State the blood parasite species.
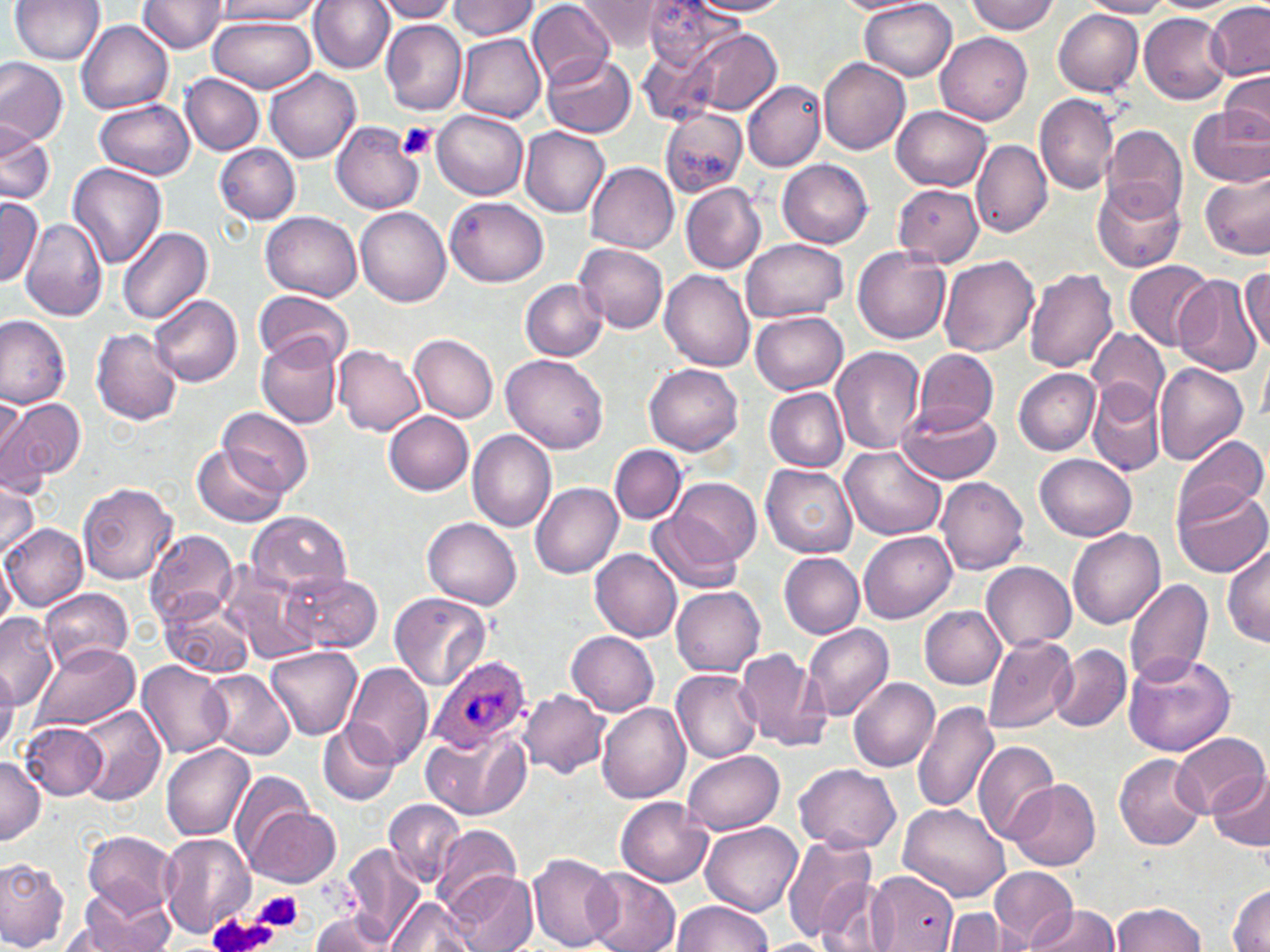
Plasmodium ovale.

Summary:
  - Coordinate format: approximate bounding boxes as (x1,y1)-(x2,y2) corner pairs in pixels
  - Platelet locations: (398,120)-(438,161), (256,889)-(303,931), (207,911)-(277,952)
  - Plasmodium ovale-infected red blood cell locations: (430,654)-(533,753)
  - Uninfected red blood cell locations: (10,0)-(105,65), (212,0)-(322,22), (310,0)-(396,73), (375,0)-(460,22), (640,0)-(735,74), (689,0)-(794,16), (859,0)-(958,80), (966,0)-(1060,36), (1082,0)-(1174,17), (137,1)-(227,54), (447,1)-(542,42), (833,1)-(932,15), (1149,1)-(1241,12), (1204,1)-(1269,81), (528,2)-(614,88), (574,2)-(684,52), (1053,9)-(1144,96), (1137,12)-(1229,103), (208,15)-(316,93), (75,19)-(173,114), (381,19)-(467,116), (669,28)-(782,119), (455,31)-(546,121), (936,33)-(1033,124), (543,53)-(636,137), (818,57)-(910,156), (0,58)-(69,148), (264,68)-(361,164), (1220,71)-(1270,144), (181,73)-(264,156), (743,78)-(826,171), (1034,94)-(1119,194), (96,98)-(196,180), (893,105)-(991,191), (1188,108)-(1270,186), (432,109)-(528,199), (661,109)-(749,197), (0,121)-(54,206), (332,121)-(423,216), (1101,123)-(1187,221), (519,125)-(610,216), (972,138)-(1052,237), (216,143)-(302,224), (777,159)-(874,247), (585,161)-(679,254), (66,162)-(168,270), (1200,165)-(1270,260), (1093,180)-(1187,273), (892,182)-(984,268), (681,183)-(767,275), (0,197)-(42,287), (446,197)-(550,288), (355,207)-(450,308), (260,212)-(362,301), (21,218)-(108,321), (118,227)-(213,326), (739,239)-(849,324), (575,244)-(670,332), (853,248)-(951,344), (939,254)-(1040,357), (1123,260)-(1211,349), (1241,267)-(1270,353), (1024,268)-(1119,374), (660,269)-(755,373), (1174,274)-(1265,375), (520,279)-(608,360), (254,291)-(352,369), (150,294)-(243,388), (751,312)-(849,395), (0,315)-(72,409), (90,327)-(183,425), (1088,327)-(1168,412), (409,332)-(498,422), (256,333)-(342,429), (334,345)-(425,437), (830,345)-(925,454), (913,348)-(1000,434), (1258,349)-(1270,429), (501,354)-(607,455), (1154,362)-(1247,466), (644,363)-(744,456), (1013,368)-(1101,454), (1088,379)-(1165,476), (763,388)-(849,472), (0,391)-(27,478), (0,396)-(85,487), (895,400)-(1002,484), (218,407)-(313,499), (384,412)-(474,495), (466,429)-(558,533), (1173,434)-(1269,528), (194,443)-(287,528), (610,445)-(686,524), (839,446)-(946,541), (1034,453)-(1136,541), (760,464)-(858,559), (663,475)-(762,574), (935,476)-(1030,575), (0,481)-(39,562), (531,482)-(623,578), (78,483)-(178,585), (1173,484)-(1268,579), (246,511)-(353,599), (650,512)-(743,594), (423,517)-(522,610), (1,523)-(87,612), (144,528)-(241,629), (860,529)-(958,624), (1067,529)-(1165,629), (1222,544)-(1269,648), (590,549)-(683,643), (779,552)-(864,638), (0,554)-(16,631), (981,561)-(1077,651), (217,562)-(324,665), (284,572)-(380,653), (1121,577)-(1214,688), (672,586)-(766,675), (40,588)-(134,673), (389,592)-(493,693), (160,598)-(253,679), (919,604)-(1006,688), (0,612)-(60,710), (802,622)-(895,720), (565,630)-(660,716), (982,635)-(1077,733), (31,642)-(139,733), (264,645)-(362,740), (1049,646)-(1131,732), (734,648)-(830,753), (1122,651)-(1238,757), (139,661)-(231,758), (343,664)-(432,771), (0,665)-(21,753), (202,670)-(294,762), (671,670)-(762,763), (849,678)-(939,771), (519,690)-(609,778), (911,699)-(1000,815), (597,702)-(690,804), (72,704)-(165,806), (319,720)-(400,804), (20,721)-(110,800), (421,727)-(530,821), (1169,731)-(1267,817), (975,740)-(1056,846), (161,744)-(255,842), (681,750)-(785,835), (1114,753)-(1210,850), (0,756)-(45,844), (794,762)-(903,853), (1207,767)-(1270,852), (230,770)-(318,863), (1007,778)-(1101,871), (384,798)-(465,887), (617,798)-(713,886), (898,803)-(1009,901), (244,804)-(341,888), (701,818)-(803,917), (432,823)-(524,912), (82,830)-(179,918), (158,833)-(255,935), (781,834)-(881,945), (341,844)-(428,945), (527,851)-(621,951), (0,857)-(69,950), (989,867)-(1078,946), (583,869)-(681,952), (867,869)-(962,950), (451,871)-(537,950), (814,874)-(896,952), (1229,886)-(1270,951), (66,892)-(174,952), (386,895)-(480,952), (672,900)-(773,951), (1026,901)-(1122,952), (1110,902)-(1207,952), (309,911)-(397,951), (942,911)-(1029,951), (758,938)-(836,952)
  - Image size: 1270×952 pixels
  - Preparation: thin blood film
  - Stain: May-Grünwald-Giemsa
  - Field of view: single
  - Magnification: 1000x
  - Modality: light microscopy